Classify this cell by malaria status.
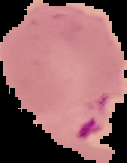

Parasitized.

image size = 127×163 pixels
image type = cell region segmented out of the field of view; surrounding area masked to black
preparation = thin blood film